Assess this cell for malaria.
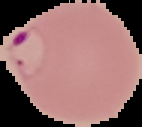
Parasitized.

Summary:
  - Preparation: thin blood smear
  - Image type: segmented cell region with the area outside set to black
  - Image size: 142×127 pixels